Give the preparation type.
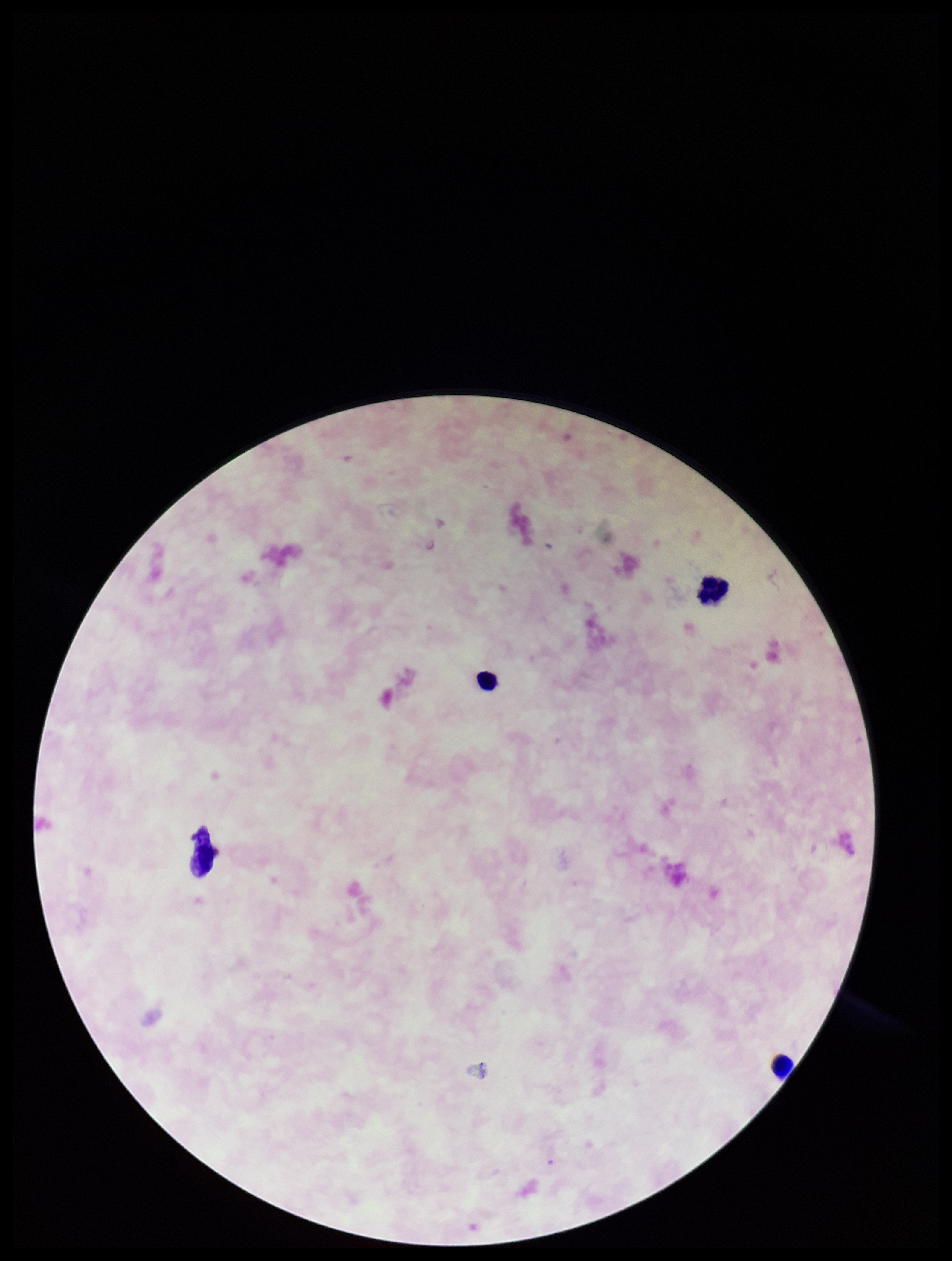
It is a thick blood smear.

Parasite count: 0. Giemsa stain. Photographed through the microscope eyepiece with a smartphone camera. Leukocyte count: 4. Plasmodium parasites: none identified. Patient malaria status: negative. Image is 952×1261 pixels. One field from this slide.